Give the extent of all uninfected red blood cells.
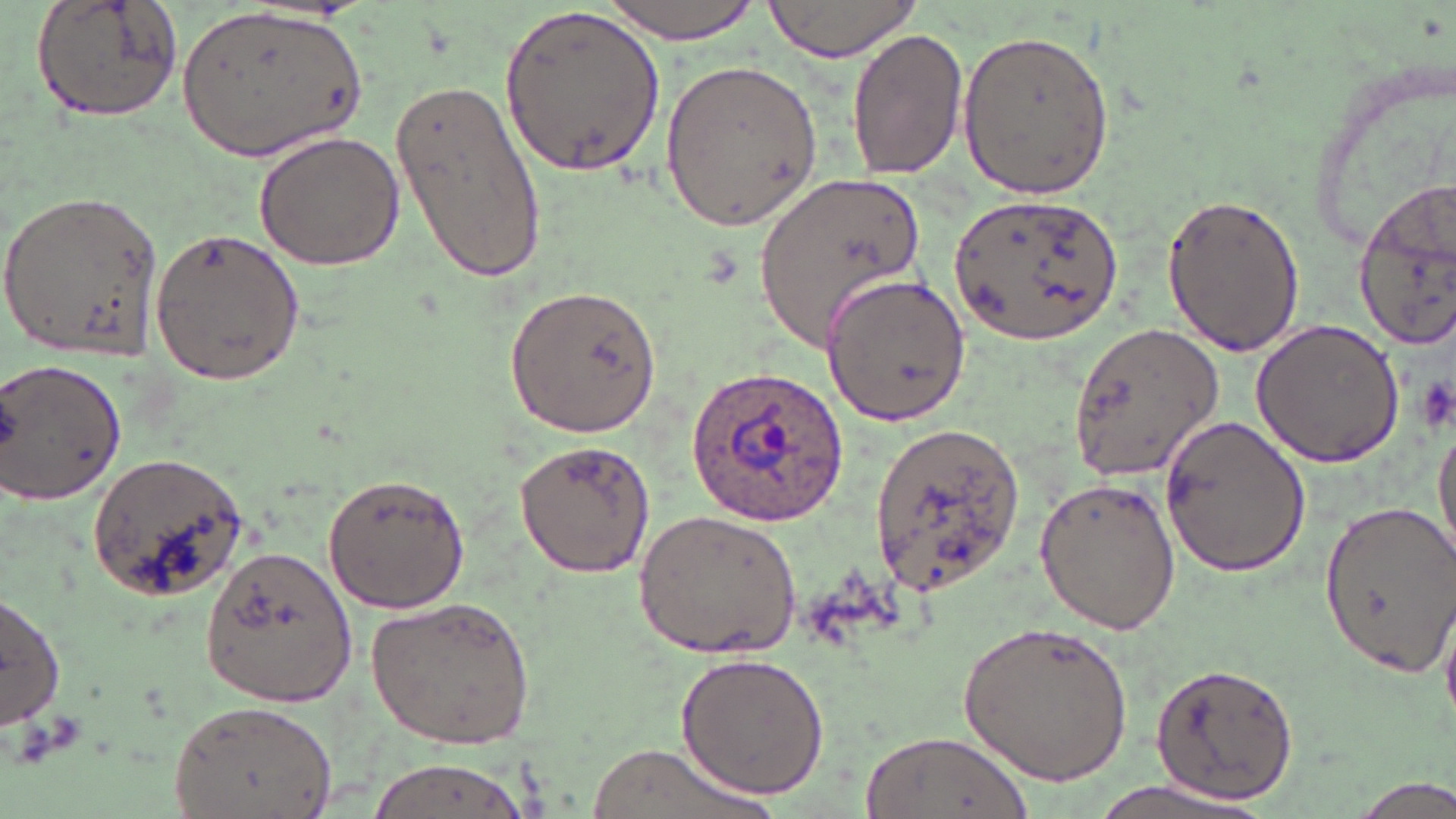

Approximate bounding boxes as named x1/y1/x2/y2 corners in pixels.
Uninfected red blood cells: (x1=31, y1=0, x2=185, y2=122), (x1=599, y1=0, x2=765, y2=41), (x1=761, y1=0, x2=925, y2=62), (x1=499, y1=1, x2=665, y2=180), (x1=177, y1=6, x2=369, y2=161), (x1=846, y1=27, x2=968, y2=182), (x1=955, y1=27, x2=1114, y2=199), (x1=660, y1=59, x2=821, y2=233), (x1=389, y1=72, x2=548, y2=282), (x1=253, y1=130, x2=406, y2=272), (x1=757, y1=171, x2=930, y2=354), (x1=1350, y1=175, x2=1456, y2=346), (x1=0, y1=188, x2=164, y2=365), (x1=949, y1=191, x2=1123, y2=348), (x1=1161, y1=191, x2=1310, y2=358), (x1=147, y1=225, x2=307, y2=387), (x1=820, y1=271, x2=970, y2=427), (x1=504, y1=283, x2=664, y2=439), (x1=1250, y1=319, x2=1405, y2=468), (x1=1067, y1=321, x2=1226, y2=482), (x1=1, y1=354, x2=129, y2=509), (x1=1159, y1=414, x2=1311, y2=577), (x1=1433, y1=415, x2=1456, y2=563), (x1=868, y1=419, x2=1027, y2=600), (x1=514, y1=438, x2=656, y2=580), (x1=86, y1=452, x2=252, y2=602), (x1=320, y1=472, x2=471, y2=616), (x1=1033, y1=476, x2=1181, y2=636), (x1=1315, y1=498, x2=1456, y2=678), (x1=633, y1=506, x2=807, y2=662), (x1=202, y1=542, x2=360, y2=705), (x1=0, y1=590, x2=65, y2=730), (x1=365, y1=595, x2=536, y2=748), (x1=956, y1=618, x2=1133, y2=788), (x1=676, y1=653, x2=829, y2=799), (x1=1151, y1=662, x2=1300, y2=804), (x1=166, y1=698, x2=339, y2=819), (x1=863, y1=731, x2=1029, y2=819), (x1=583, y1=742, x2=780, y2=819), (x1=361, y1=755, x2=536, y2=819), (x1=1077, y1=777, x2=1276, y2=819), (x1=1347, y1=777, x2=1455, y2=818).

Plasmodium ovale-infected red blood cell locations = approximate bounding boxes as named x1/y1/x2/y2 corners in pixels: (x1=686, y1=364, x2=850, y2=526)
slide-level diagnosis = Plasmodium ovale
magnification = 1000x
preparation = thin blood film
modality = optical microscopy
stain = May-Grünwald-Giemsa
field of view = one of a larger specimen
platelet locations = approximate bounding boxes as named x1/y1/x2/y2 corners in pixels: (x1=1413, y1=373, x2=1455, y2=435)
image size = 1456×819 pixels